Report the malaria status of this cell.
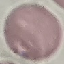
Uninfected.

Giemsa stain. Cell patch, automatically extracted from a larger field of view and resized to 64 × 64 pixels. Acquired by smartphone through the microscope eyepiece. Thin smear of blood.